Comment on the morphology of the erythrocytes.
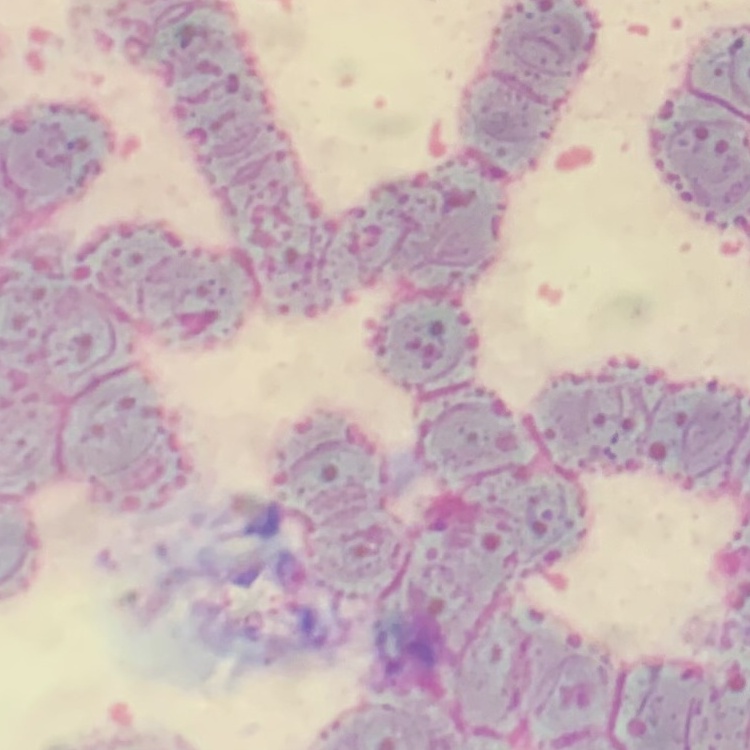

They show rouleaux formation.

preparation = thin blood smear
stain = Field's or Giemsa
image type = square crop of a larger photomicrograph